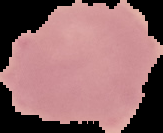
image type = segmented cell region with the area outside set to black
result = no Plasmodium parasites detected
image size = 163×133 pixels
preparation = thin blood film